Outline each blood parasite and name the species.
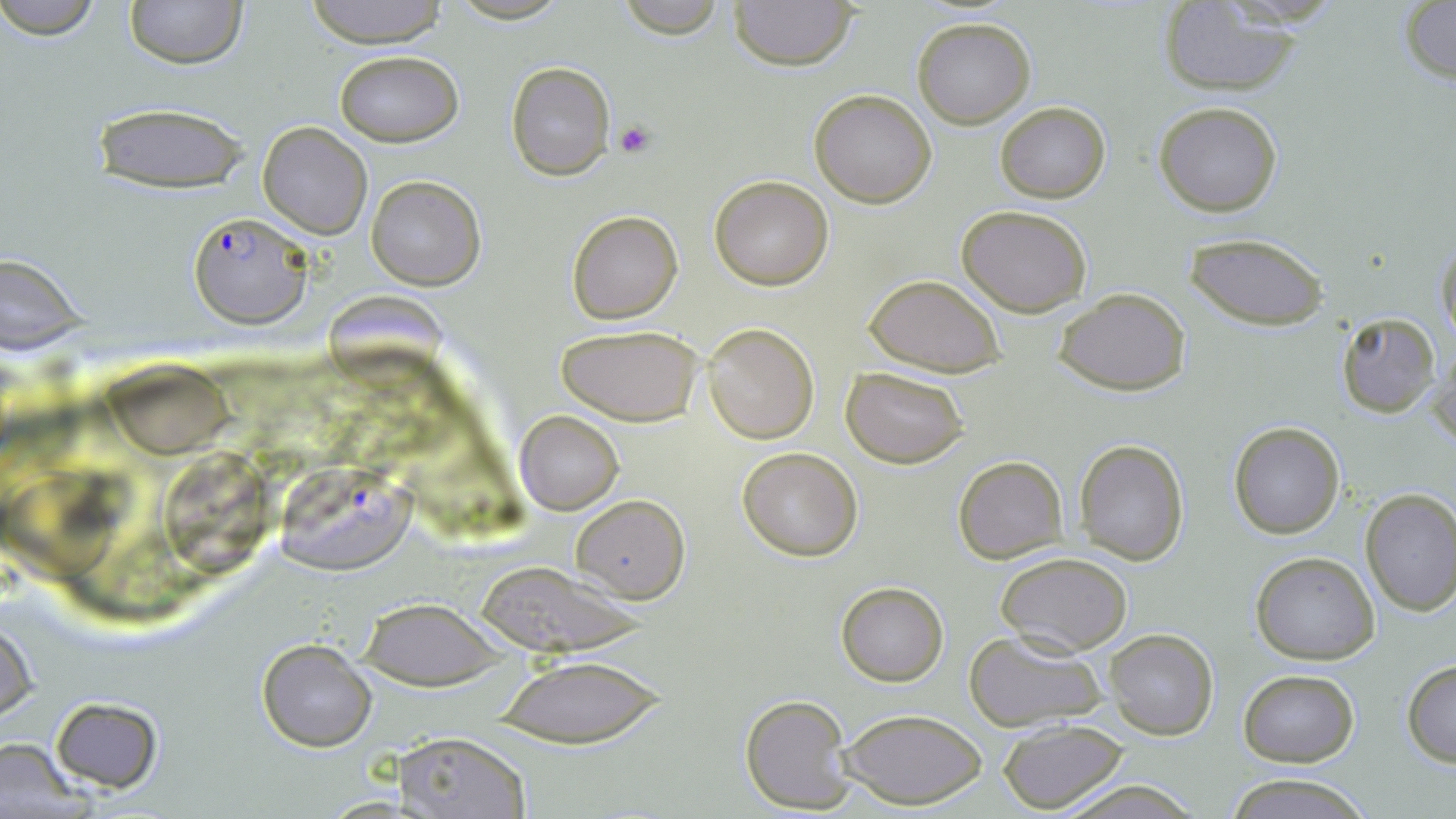

Approximate bounding boxes as (x1,y1)-(x2,y2) corner pairs in pixels.
Plasmodium falciparum-infected red blood cells: (187,209)-(313,329), (277,471)-(424,577).
No Plasmodium ovale, Plasmodium malariae, Plasmodium vivax, Babesia divergens, or Trypanosoma brucei observed.

Platelet locations: (614,120)-(656,158). Uninfected red blood cell locations: (0,0)-(108,42), (123,0)-(248,69), (300,0)-(452,47), (611,0)-(731,39), (729,1)-(857,70), (1157,2)-(1309,96), (1401,2)-(1455,86), (912,17)-(1036,128), (334,50)-(463,148), (505,61)-(615,179), (809,90)-(936,208), (1154,100)-(1283,217), (994,101)-(1110,202), (91,103)-(254,195), (259,121)-(373,239), (709,174)-(835,291), (367,175)-(485,291), (957,204)-(1093,315), (568,211)-(683,324), (1188,234)-(1330,331), (1434,236)-(1456,349), (0,255)-(92,357), (863,273)-(1005,376), (1055,287)-(1191,396), (328,289)-(446,391), (1337,312)-(1441,417), (702,322)-(818,444), (556,324)-(703,426), (1429,346)-(1456,453), (103,363)-(228,460), (840,365)-(970,468), (514,410)-(624,515), (1227,420)-(1346,539), (1073,439)-(1189,565), (164,446)-(267,585), (737,447)-(862,561), (954,455)-(1068,565), (7,463)-(126,586), (1360,490)-(1456,615), (573,494)-(689,601), (1250,551)-(1379,665), (996,552)-(1133,656), (477,566)-(649,654), (836,581)-(948,686), (358,597)-(502,690), (1,618)-(37,725), (1104,629)-(1219,740), (964,631)-(1106,732), (256,638)-(377,752), (490,655)-(667,744), (1402,658)-(1456,766), (1237,668)-(1358,766), (740,693)-(854,813), (50,696)-(166,794), (837,708)-(987,809), (996,719)-(1131,814), (389,731)-(532,818), (0,737)-(90,814), (1225,772)-(1370,819), (1054,776)-(1206,818). Slide-level diagnosis: Plasmodium falciparum. Captured at 1000x magnification. Image is 1456×819 pixels. May-Grünwald-Giemsa-stained preparation. Thin blood smear. Optical microscopy. Single field of view.